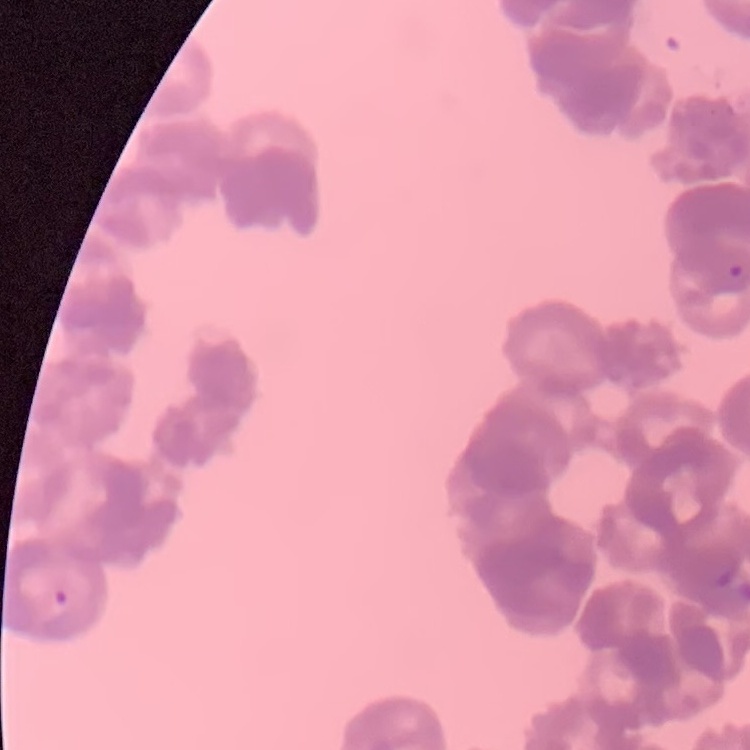
The erythrocytes exhibit rouleaux formation. Thin blood smear. One tile cut from a larger photomicrograph. Stained with either Field's or Giemsa.